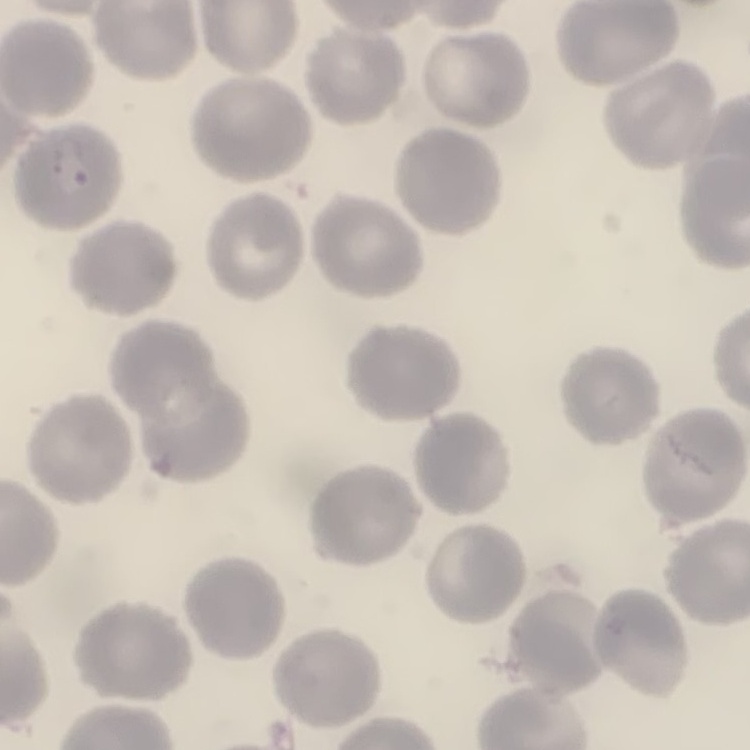

erythrocyte morphology = no rouleaux formation
image type = one tile cut from a larger photomicrograph
stain = Field's or Giemsa
preparation = thin peripheral smear